Classify this cell by malaria status.
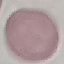
Uninfected.

stain = Giemsa
image type = cell patch, automatically extracted from a larger field of view and resized to 64 × 64 pixels
preparation = thin smear
capture = smartphone through the microscope eyepiece